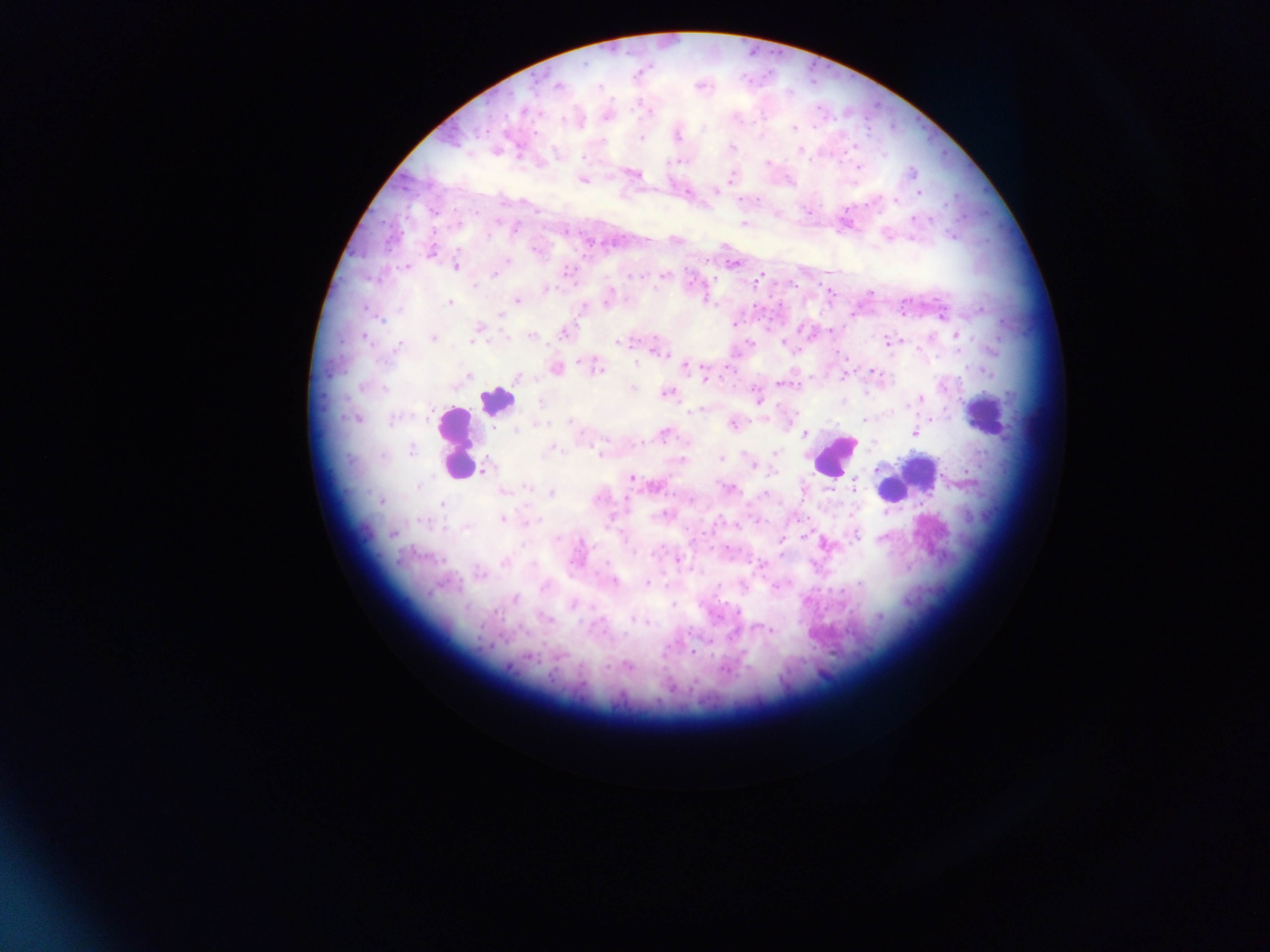
Approximate centers as [x, y] in pixels. Leukocyte locations: [495, 400], [985, 416], [455, 443], [834, 455], [921, 469], [891, 490]. Plasmodium parasite locations: [558, 86], [600, 87], [522, 111], [650, 112], [562, 119], [703, 128], [793, 128], [535, 132], [677, 136], [640, 138], [601, 141], [731, 148], [583, 157], [809, 161], [767, 163], [858, 167], [912, 172], [635, 175], [730, 178], [582, 180], [716, 191], [688, 192], [919, 193], [742, 200], [757, 200], [894, 200], [947, 203], [806, 210], [913, 219], [497, 220], [458, 224], [743, 224], [516, 229], [565, 232], [487, 236], [952, 236], [535, 250], [431, 251], [507, 260], [734, 264], [405, 267], [454, 267], [567, 271], [495, 274], [664, 275], [760, 276], [638, 277], [473, 286], [546, 289], [829, 292], [870, 293], [705, 300], [517, 301], [450, 302], [605, 303], [400, 309], [981, 309], [501, 315], [941, 315], [381, 319], [734, 324], [479, 326], [801, 329], [831, 330], [564, 333], [531, 336], [957, 336], [364, 338], [433, 338], [472, 341], [619, 342], [750, 342], [887, 342], [783, 343], [398, 347], [992, 350], [657, 351], [580, 363], [636, 363], [686, 366], [556, 369], [598, 370], [871, 371], [986, 372], [468, 375], [844, 377], [516, 378], [704, 379], [782, 383], [454, 387], [632, 388], [385, 389], [667, 393], [755, 394], [922, 398], [541, 401], [758, 402], [907, 408], [692, 412], [429, 417], [765, 418], [355, 419], [931, 419], [393, 420], [864, 420], [570, 421], [538, 425], [733, 425], [515, 431], [664, 433], [915, 433], [805, 434], [555, 448], [594, 450], [412, 451], [775, 453], [383, 455], [720, 459], [485, 466], [752, 466], [878, 469], [773, 473], [631, 478], [853, 484], [418, 487], [527, 488], [727, 488], [503, 491], [550, 492], [766, 494], [381, 501], [442, 504], [664, 514], [503, 519], [531, 521], [758, 521], [423, 522], [737, 525], [466, 527], [393, 533], [856, 535], [804, 536], [882, 538], [557, 539], [781, 540], [523, 545], [633, 552], [678, 561], [505, 562], [762, 565], [614, 582], [647, 583], [860, 584], [774, 586], [543, 587], [515, 600], [574, 604], [673, 604], [737, 612], [879, 617], [551, 619], [631, 620], [646, 622], [759, 628], [771, 630], [689, 633], [692, 652], [629, 666], [607, 668], [726, 670]. Mobile-phone photograph taken through the microscope. Image is 1270×952 pixels. Sample from Ghana. Thick blood smear. Single field of view.